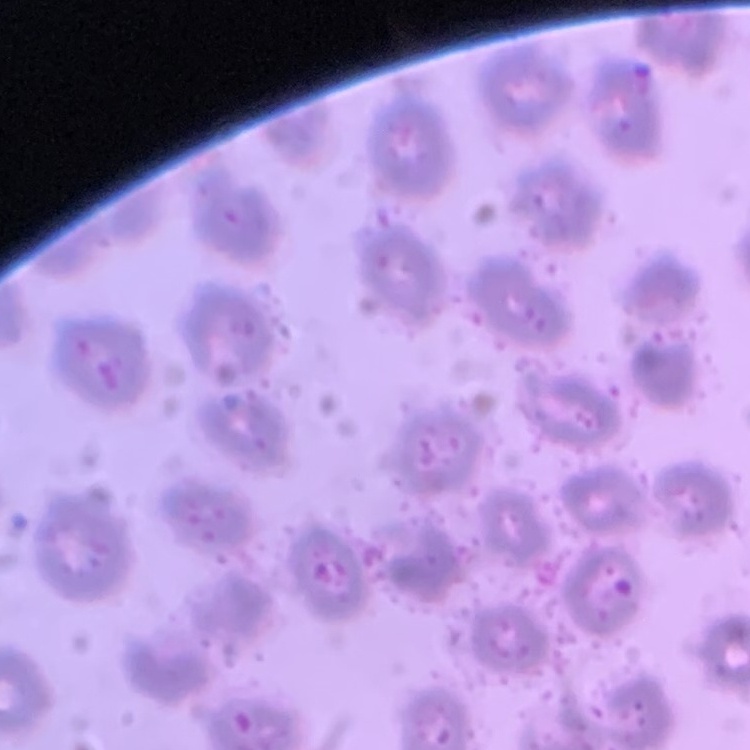
The erythrocytes exhibit no rouleaux formation. Square crop of a larger photomicrograph. Thin peripheral smear. Stained with either Field's or Giemsa.